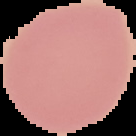
Summary:
  - Result: no malaria parasites detected
  - Preparation: thin blood film
  - Image size: 136×136 pixels
  - Image type: cell region segmented out of the field of view; surrounding area masked to black